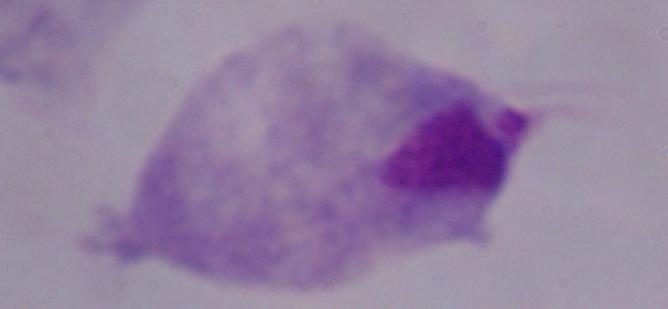
Summary:
  - Magnification: 1000x
  - Modality: photomicrograph
  - Identification: trichomonad